Identify the cell.
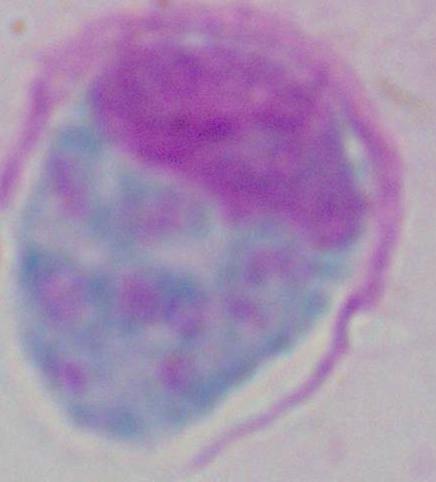
A leukocyte.

Photomicrograph. 1000x magnification.